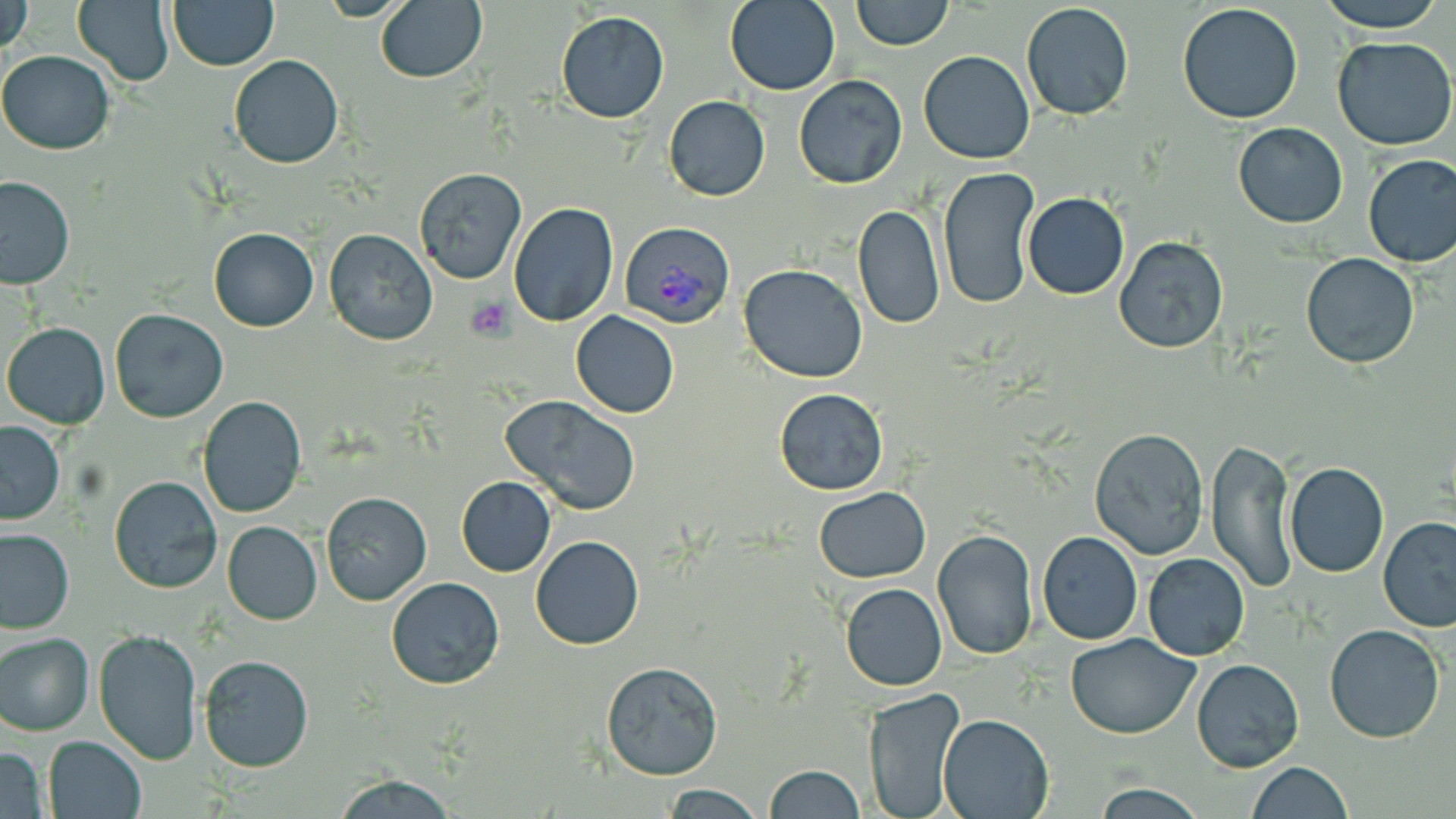

{
  "slide_level_diagnosis": "Plasmodium vivax",
  "preparation": "thin blood smear",
  "field_of_view": "one of a larger specimen",
  "platelet_locations": "approximate bounding boxes as (x1, y1, x2, y2) in pixels: (465, 295, 516, 341)",
  "image_size": "1456×819 pixels",
  "plasmodium_vivax_infected_red_blood_cell_locations": "approximate bounding boxes as (x1, y1, x2, y2) in pixels: (616, 222, 731, 328)",
  "magnification": "1000x",
  "modality": "optical microscopy",
  "uninfected_red_blood_cell_locations": "approximate bounding boxes as (x1, y1, x2, y2) in pixels: (374, 0, 487, 83), (724, 0, 841, 95), (850, 0, 954, 51), (1314, 0, 1446, 33), (2, 1, 31, 54), (72, 1, 174, 84), (168, 1, 278, 70), (1021, 2, 1136, 120), (1176, 2, 1305, 125), (555, 11, 670, 122), (1330, 34, 1456, 152), (0, 49, 115, 155), (919, 50, 1034, 165), (229, 54, 343, 169), (792, 75, 908, 189), (664, 95, 770, 202), (1234, 122, 1349, 229), (1361, 154, 1456, 268), (937, 166, 1039, 309), (411, 167, 528, 286), (0, 174, 75, 288), (1022, 192, 1130, 300), (509, 202, 618, 326), (852, 206, 944, 330), (208, 227, 318, 331), (324, 228, 440, 346), (1114, 238, 1229, 352), (1301, 253, 1419, 369), (739, 263, 868, 383), (109, 308, 230, 424), (571, 311, 680, 418), (3, 322, 110, 428), (773, 387, 890, 496), (197, 395, 307, 519), (502, 395, 641, 515), (0, 421, 66, 524), (1089, 427, 1212, 560), (1205, 437, 1297, 595), (1284, 463, 1390, 579), (109, 474, 223, 594), (456, 476, 556, 576), (814, 486, 929, 584), (321, 491, 431, 605), (1378, 516, 1456, 632), (222, 521, 323, 625), (0, 528, 74, 633), (931, 528, 1038, 660), (1036, 532, 1143, 645), (531, 536, 644, 651), (1143, 553, 1251, 660), (386, 578, 504, 689), (840, 583, 947, 691), (1324, 623, 1445, 743), (94, 628, 203, 764), (0, 633, 94, 736), (1065, 633, 1202, 739), (197, 653, 315, 773), (1190, 657, 1305, 772), (600, 662, 723, 780), (863, 685, 965, 819), (938, 713, 1053, 819), (41, 735, 146, 818), (0, 745, 49, 818), (1245, 761, 1354, 819), (762, 764, 865, 819), (330, 772, 458, 818), (661, 782, 767, 818)",
  "stain": "May-Grünwald-Giemsa"
}